Report the malaria status of this cell.
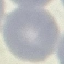
Uninfected.

Summary:
  - Capture: smartphone through the microscope eyepiece
  - Image type: automatically extracted cell patch, resized to 64 × 64 pixels
  - Preparation: thin blood film
  - Stain: Giemsa